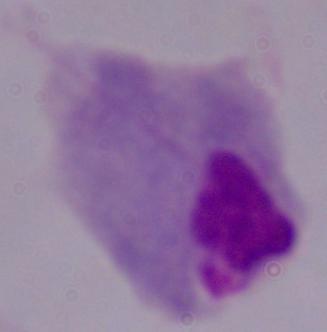
Photomicrograph. A trichomonad is shown. Captured at 1000x magnification.